Describe the morphology of the red blood cells.
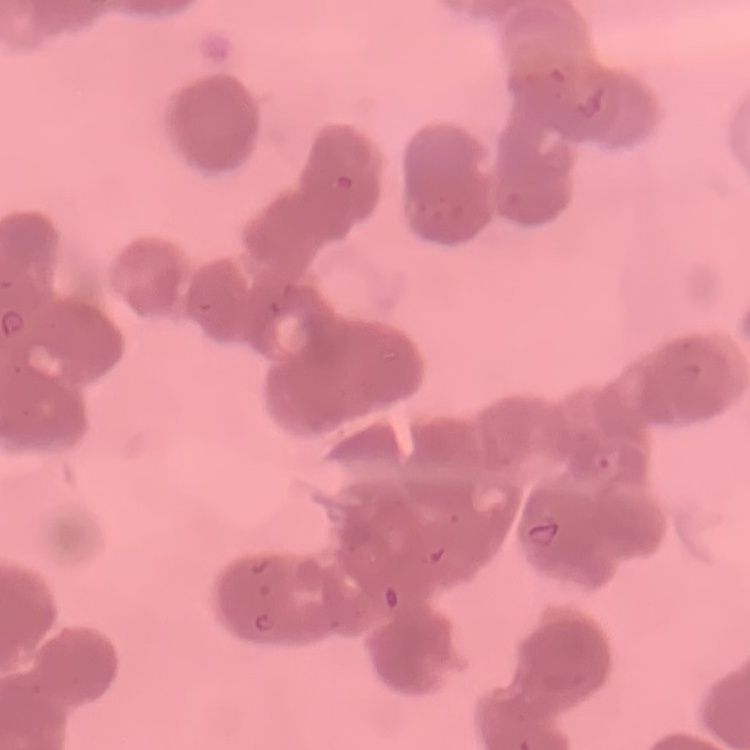
They show rouleaux formation.

Summary:
  - Stain: Field's or Giemsa
  - Image type: square crop of a larger photomicrograph
  - Preparation: thin peripheral smear